Classify this cell by malaria status.
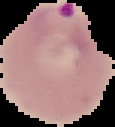

It is parasitized.

image type = cell region segmented out of the field of view; surrounding area masked to black
image size = 115×127 pixels
preparation = thin blood smear